Find the cells and give the type of each one.
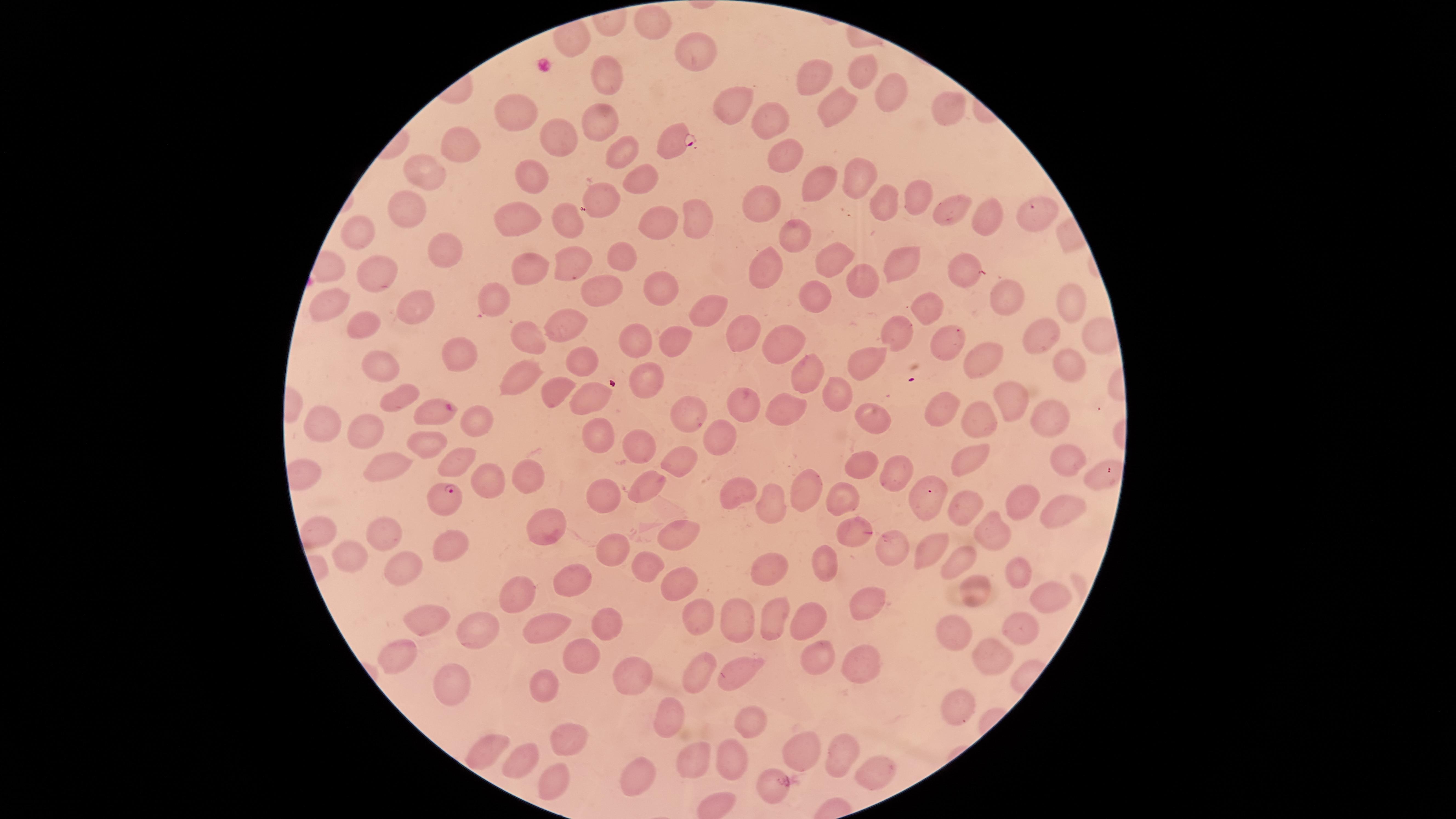

Approximate marker points as [x, y] in pixels.
Parasitized red blood cells: [673, 141], [442, 407], [443, 496].
Uninfected red blood cells: [649, 22], [694, 49], [612, 74], [812, 74], [864, 74], [889, 91], [731, 101], [840, 103], [952, 111], [516, 115], [767, 117], [599, 118], [551, 132], [460, 147], [615, 150], [784, 153], [533, 170], [424, 175], [863, 176], [641, 178], [817, 185], [600, 193], [916, 193], [768, 200], [887, 201], [408, 208], [951, 210], [1033, 210], [521, 214], [699, 217], [982, 217], [570, 219], [647, 222], [793, 231], [358, 233], [444, 248], [621, 257], [900, 257], [576, 260], [841, 261], [966, 264], [532, 268], [764, 270], [382, 274], [862, 280], [662, 289], [1008, 291], [604, 292], [818, 299], [496, 302], [1074, 302], [711, 307], [333, 308], [414, 310], [919, 312], [568, 324], [365, 327], [743, 330], [1038, 334], [528, 337], [903, 337], [678, 338], [640, 339], [777, 339], [944, 340], [461, 349], [1069, 356], [582, 359], [381, 361], [983, 364], [873, 365], [806, 369], [651, 377], [519, 379], [835, 389], [558, 391], [588, 393], [1011, 393], [404, 396], [683, 409], [941, 409], [786, 410], [979, 413], [1047, 414], [746, 415], [875, 415], [477, 421], [325, 426], [597, 434], [357, 435], [641, 439], [716, 439], [424, 445], [968, 452], [677, 457], [1070, 457], [855, 461], [459, 462], [377, 466], [896, 469], [1098, 476], [532, 477], [496, 478], [647, 480], [602, 489], [807, 489], [739, 492], [839, 498], [1030, 498], [772, 503], [926, 505], [962, 506], [1064, 507], [551, 523], [994, 530], [377, 531], [675, 535], [848, 542], [451, 543], [614, 545], [928, 547], [896, 549], [356, 553], [966, 555], [652, 559], [407, 564], [770, 567], [819, 572], [1014, 573], [567, 583], [681, 583], [971, 591], [517, 596], [1049, 597], [865, 603], [423, 613], [703, 615], [773, 615], [610, 616], [735, 621], [1020, 622], [481, 624], [547, 628], [813, 631], [958, 634], [819, 651], [991, 653], [390, 655], [582, 662], [858, 662], [703, 670], [628, 672], [742, 672], [453, 681], [541, 684], [963, 703], [670, 717], [745, 724], [568, 733], [485, 745], [802, 746], [847, 756], [734, 757], [522, 761], [695, 764], [870, 767], [643, 776], [550, 780], [775, 782].
No white blood cells identified.

Giemsa-stained preparation. Thin blood film. Circular visible region. Image is 1456×819 pixels. One field of view of the specimen. Species: Plasmodium falciparum. Smartphone photograph through the microscope eyepiece.